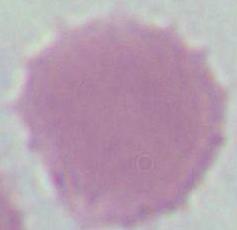
identification: red blood cell
magnification: 1000x
modality: micrograph